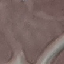

Summary:
  - Malaria status: uninfected
  - Capture: smartphone camera at the microscope eyepiece
  - Preparation: thin blood film
  - Image type: automatically extracted cell patch, resized to 64 × 64 pixels
  - Stain: Giemsa